Classify this cell by malaria status.
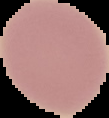

Uninfected.

Image is 109×118 pixels. Segmented cell region on a black background. From a thin blood film.